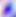

modality = micrograph
identification = Toxoplasma gondii
magnification = 400x